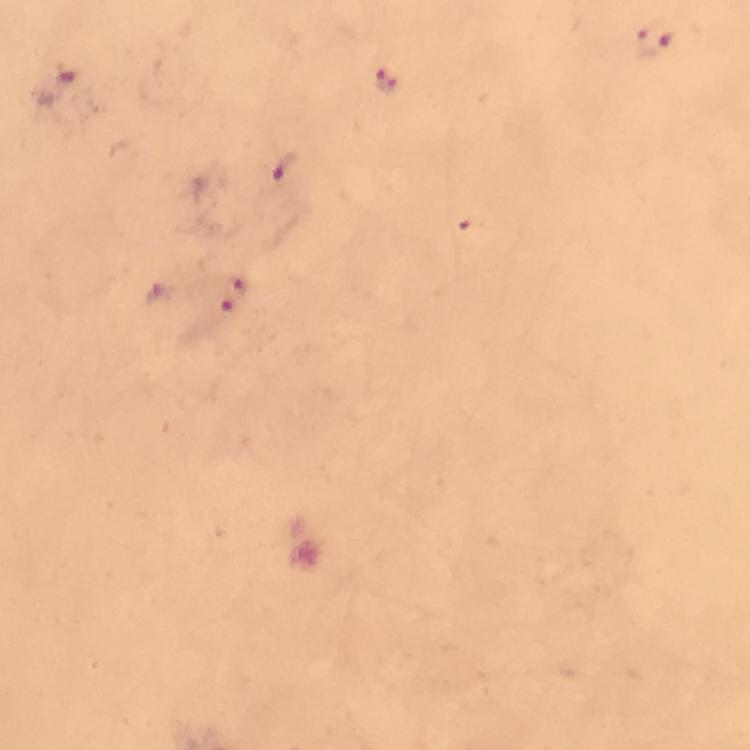 Approximate centers as {x, y} in pixels. Malaria parasite locations: {654, 40}, {386, 80}, {57, 84}, {286, 167}, {464, 226}, {240, 282}, {229, 306}. A crop from one field of view. 100x magnification. Giemsa stain. Immersion oil was used. From a malaria diagnostic workup. Thick blood smear. Image is 750×750 pixels. Photographed with a smartphone mounted on the microscope.